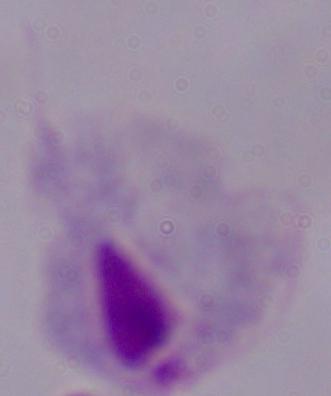

modality: photomicrograph
magnification: 1000x
identification: trichomonad